Identify the preparation type.
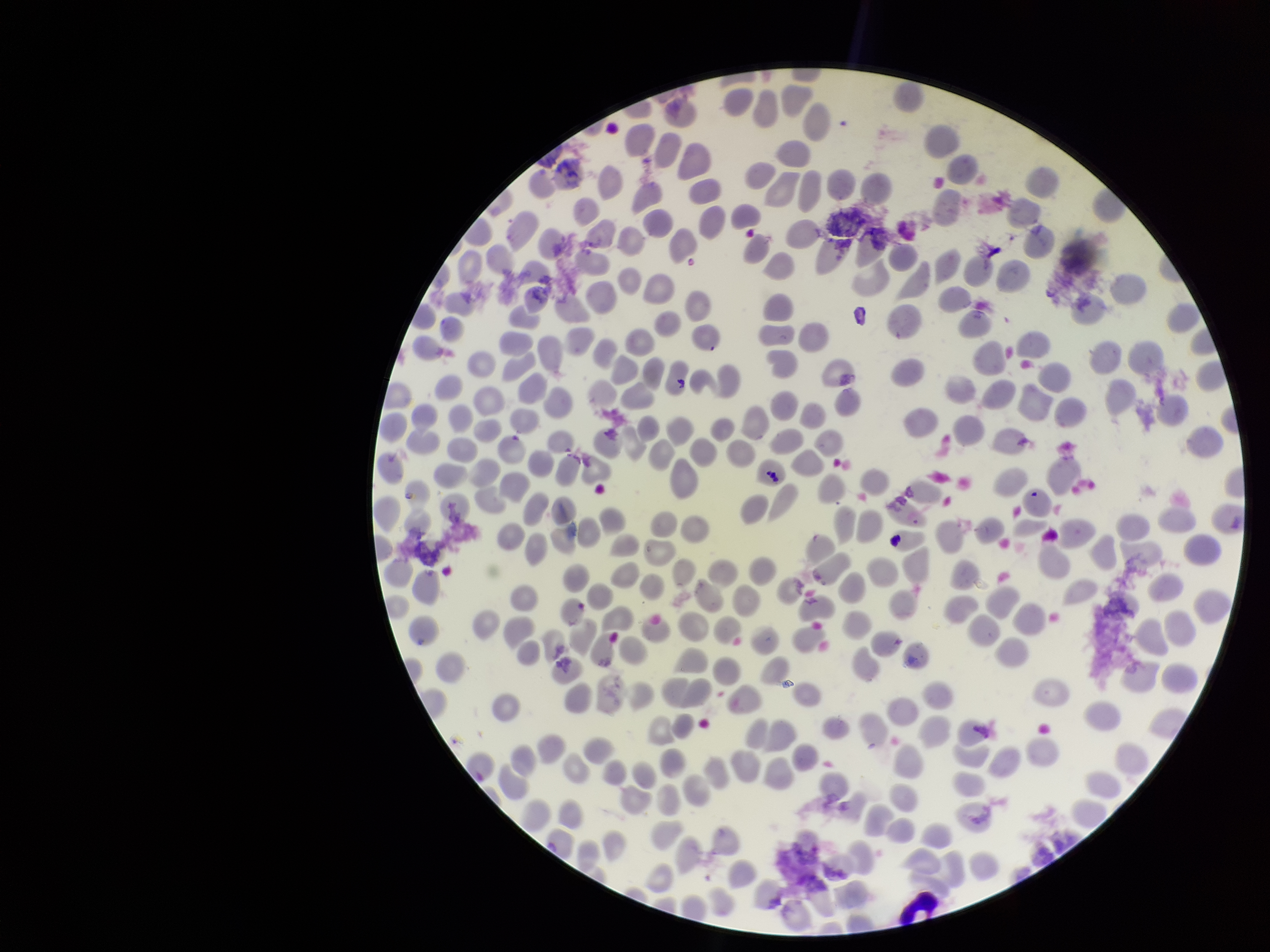

A thin smear.

{
  "parasitized_red_blood_cells": "none seen",
  "species_reported_for_this_patient": "Plasmodium vivax",
  "capture": "smartphone photograph through the microscope eyepiece",
  "parasitized_red_blood_cell_count": 0,
  "patient_malaria_status": "positive",
  "field_of_view": "one from this slide",
  "red_blood_cell_count": 243,
  "image_size": "1270×952 pixels",
  "stain": "Giemsa"
}